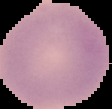
preparation = thin blood film
result = negative for Plasmodium parasites
image type = segmented cell region with the area outside set to black
image size = 112×109 pixels